Give the position of every Plasmodium parasite visible.
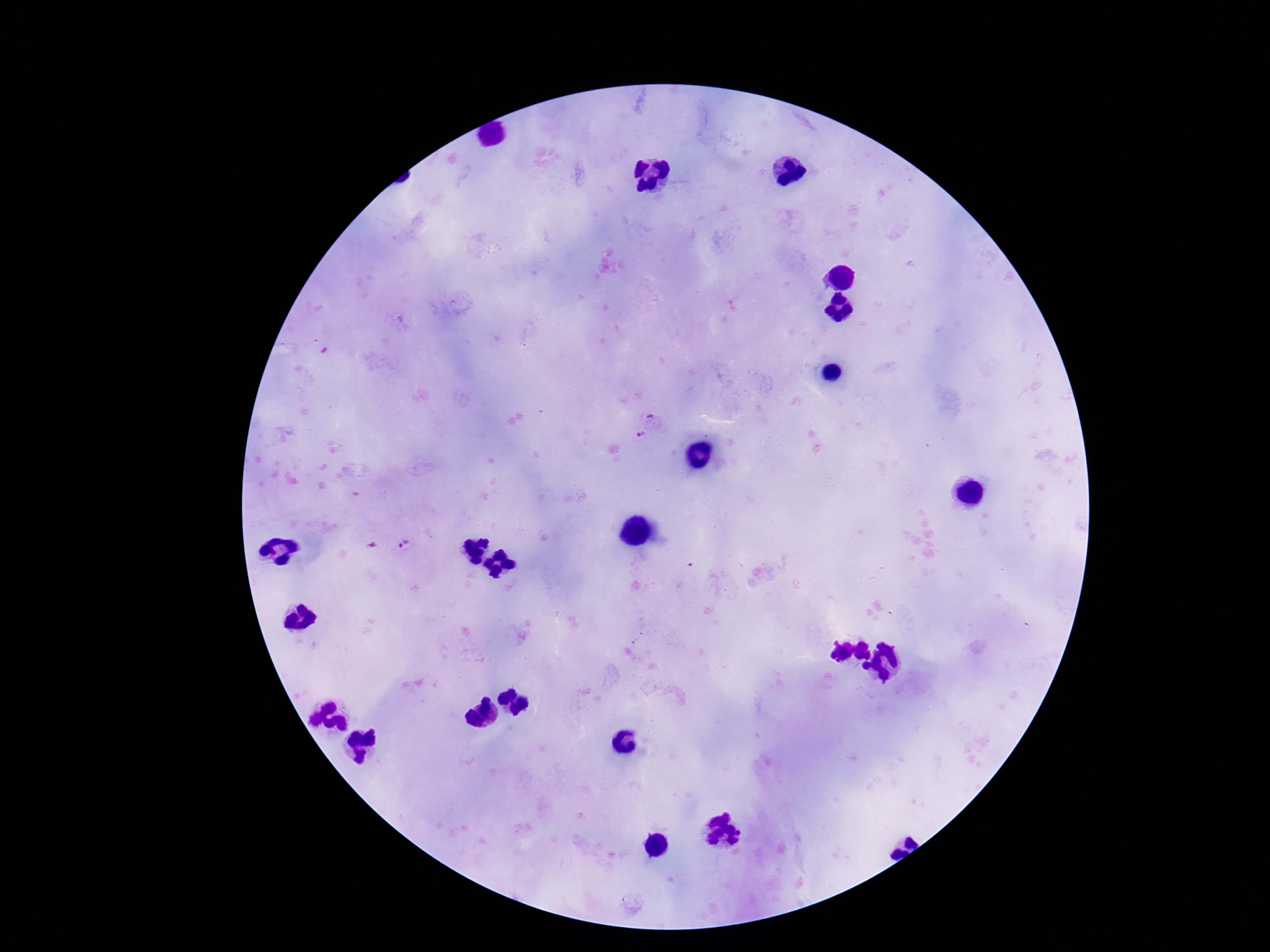

Approximate centers as (x, y) in pixels.
Plasmodium parasites: (651, 417), (641, 435), (404, 544).

field of view = one from this slide
magnification = 100x
patient malaria status = positive
preparation = thick blood film
capture = smartphone camera through the microscope eyepiece
stain = Giemsa
image size = 1270×952 pixels